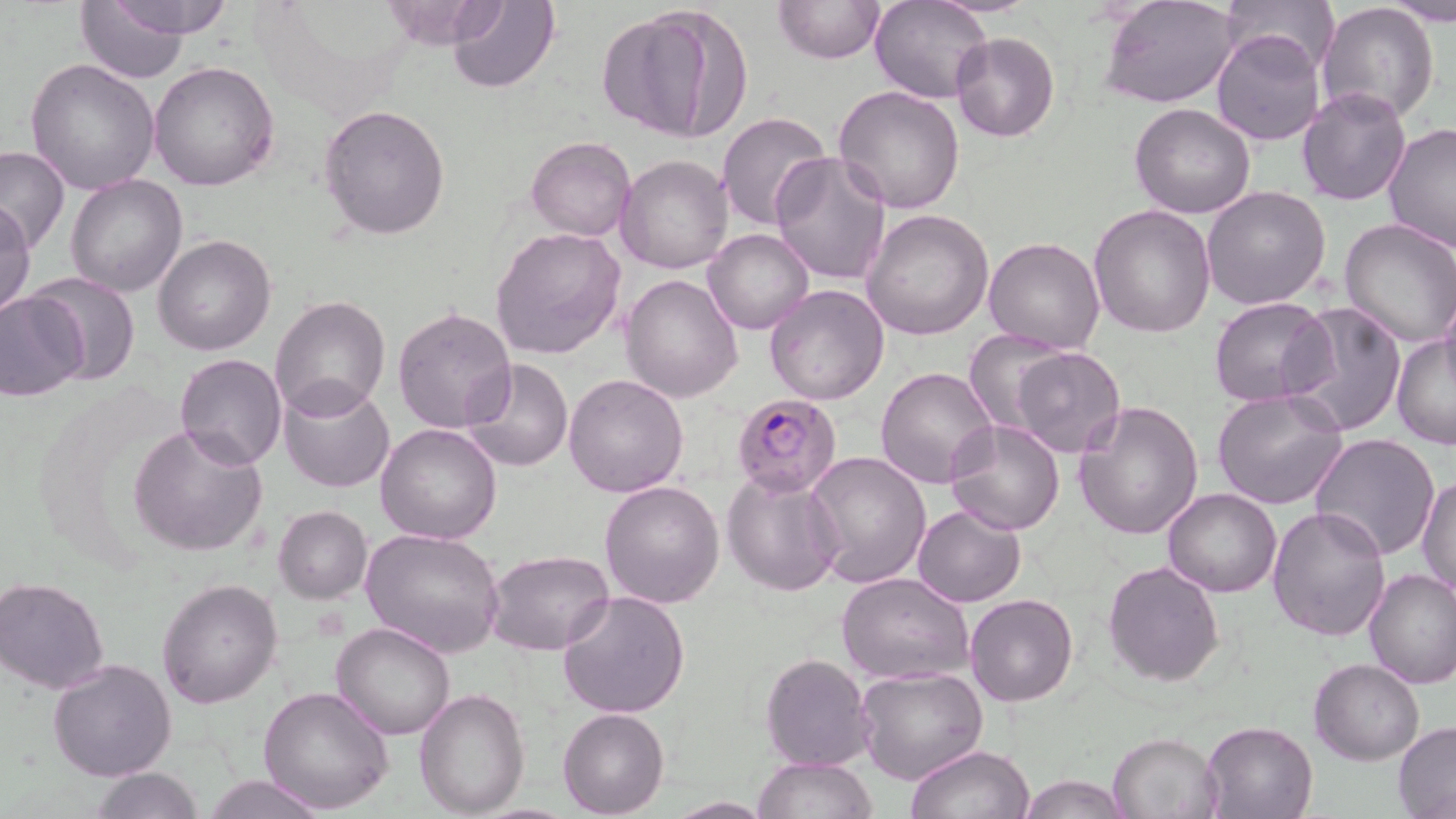

slide-level diagnosis = Plasmodium falciparum
magnification = 1000x
image size = 1456×819 pixels
modality = light microscopy
stain = May-Grünwald-Giemsa
uninfected red blood cell locations = approximate bounding boxes as named x1/y1/x2/y2 corners in pixels: (x1=100, y1=0, x2=239, y2=41), (x1=871, y1=0, x2=994, y2=104), (x1=1219, y1=0, x2=1342, y2=76), (x1=446, y1=1, x2=561, y2=93), (x1=771, y1=1, x2=886, y2=65), (x1=1316, y1=1, x2=1440, y2=125), (x1=1383, y1=1, x2=1456, y2=23), (x1=74, y1=2, x2=189, y2=83), (x1=600, y1=2, x2=748, y2=142), (x1=1100, y1=2, x2=1240, y2=108), (x1=1211, y1=29, x2=1326, y2=146), (x1=950, y1=31, x2=1059, y2=142), (x1=27, y1=58, x2=161, y2=195), (x1=148, y1=62, x2=279, y2=193), (x1=834, y1=86, x2=965, y2=213), (x1=1297, y1=88, x2=1410, y2=206), (x1=1130, y1=103, x2=1256, y2=219), (x1=318, y1=104, x2=452, y2=239), (x1=716, y1=110, x2=833, y2=230), (x1=1382, y1=123, x2=1456, y2=252), (x1=526, y1=135, x2=636, y2=240), (x1=0, y1=144, x2=69, y2=255), (x1=770, y1=152, x2=892, y2=285), (x1=616, y1=154, x2=735, y2=274), (x1=65, y1=175, x2=189, y2=298), (x1=1201, y1=186, x2=1332, y2=310), (x1=0, y1=197, x2=36, y2=320), (x1=1089, y1=203, x2=1217, y2=339), (x1=863, y1=208, x2=994, y2=340), (x1=1338, y1=219, x2=1456, y2=348), (x1=491, y1=226, x2=628, y2=360), (x1=703, y1=227, x2=813, y2=335), (x1=984, y1=235, x2=1105, y2=355), (x1=152, y1=236, x2=275, y2=357), (x1=25, y1=272, x2=141, y2=386), (x1=622, y1=274, x2=744, y2=403), (x1=764, y1=284, x2=891, y2=405), (x1=0, y1=289, x2=90, y2=402), (x1=1439, y1=294, x2=1456, y2=398), (x1=1208, y1=295, x2=1336, y2=408), (x1=272, y1=296, x2=391, y2=419), (x1=1281, y1=299, x2=1408, y2=436), (x1=392, y1=307, x2=517, y2=433), (x1=961, y1=331, x2=1075, y2=437), (x1=1390, y1=336, x2=1455, y2=449), (x1=1006, y1=347, x2=1127, y2=459), (x1=174, y1=353, x2=287, y2=470), (x1=462, y1=359, x2=573, y2=473), (x1=876, y1=365, x2=999, y2=487), (x1=563, y1=374, x2=689, y2=497), (x1=278, y1=378, x2=395, y2=493), (x1=1212, y1=389, x2=1351, y2=511), (x1=1073, y1=399, x2=1204, y2=541), (x1=944, y1=419, x2=1068, y2=536), (x1=129, y1=422, x2=268, y2=556), (x1=376, y1=423, x2=502, y2=545), (x1=1310, y1=432, x2=1442, y2=560), (x1=803, y1=450, x2=931, y2=589), (x1=722, y1=467, x2=846, y2=595), (x1=1418, y1=475, x2=1456, y2=600), (x1=600, y1=480, x2=726, y2=609), (x1=1163, y1=489, x2=1282, y2=598), (x1=912, y1=503, x2=1026, y2=606), (x1=273, y1=506, x2=371, y2=603), (x1=1267, y1=506, x2=1392, y2=642), (x1=359, y1=527, x2=505, y2=659), (x1=485, y1=549, x2=616, y2=657), (x1=1102, y1=560, x2=1225, y2=686), (x1=1363, y1=568, x2=1456, y2=690), (x1=837, y1=570, x2=973, y2=683), (x1=1, y1=575, x2=113, y2=693), (x1=156, y1=577, x2=282, y2=707), (x1=557, y1=589, x2=691, y2=720), (x1=966, y1=593, x2=1078, y2=707), (x1=331, y1=620, x2=455, y2=739), (x1=759, y1=653, x2=875, y2=771), (x1=47, y1=657, x2=176, y2=780), (x1=1309, y1=658, x2=1425, y2=765), (x1=855, y1=665, x2=988, y2=784), (x1=258, y1=686, x2=395, y2=815), (x1=413, y1=687, x2=532, y2=817), (x1=558, y1=708, x2=669, y2=818), (x1=1201, y1=720, x2=1320, y2=818), (x1=1392, y1=720, x2=1456, y2=816), (x1=1108, y1=731, x2=1223, y2=819), (x1=906, y1=744, x2=1035, y2=818), (x1=752, y1=755, x2=876, y2=818), (x1=90, y1=767, x2=203, y2=819), (x1=204, y1=774, x2=328, y2=818), (x1=1017, y1=775, x2=1130, y2=818), (x1=664, y1=798, x2=774, y2=817)
field of view = one of a larger specimen
preparation = thin blood smear
Plasmodium falciparum-infected red blood cell locations = approximate bounding boxes as named x1/y1/x2/y2 corners in pixels: (x1=731, y1=392, x2=843, y2=497)